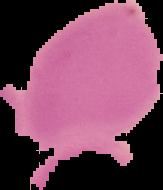
Image is 163×190 pixels. From a thin blood film. Malaria status: uninfected. Cell region segmented out of the field of view; the surrounding area is masked to black.